Classify the preparation.
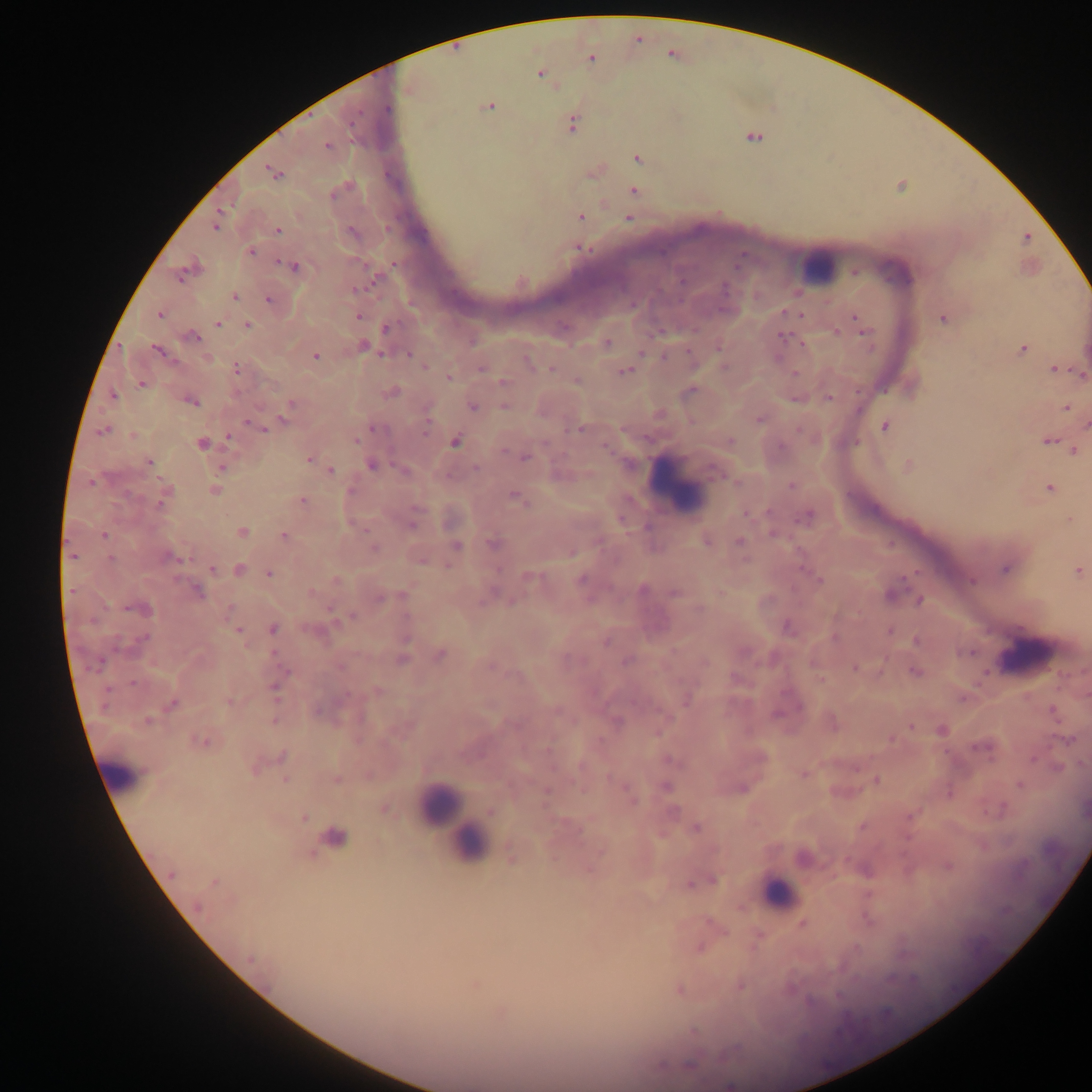

Thick blood film.

Approximate centers as x y in pixels. Leukocyte locations: 819 266; 679 483; 1025 656; 124 774; 439 805; 460 827; 469 844; 778 891. Malaria parasite locations: 591 59; 540 75; 487 107; 389 109; 350 124; 572 125; 754 137; 327 146; 638 159; 273 173; 634 192; 581 217; 628 219; 215 226; 278 230; 1027 238; 580 248; 251 252; 293 266; 855 271; 182 276; 374 280; 682 280; 725 289; 357 290; 234 297; 269 300; 786 313; 160 314; 799 314; 358 316; 857 318; 943 319; 218 324; 861 324; 248 326; 386 328; 837 331; 865 332; 192 336; 783 337; 607 343; 363 346; 718 348; 1023 350; 158 351; 641 353; 382 354; 408 354; 315 356; 664 357; 207 359; 528 363; 425 367; 237 368; 482 368; 552 368; 1054 368; 625 371; 794 374; 1081 374; 449 377; 504 381; 577 381; 141 383; 391 392; 113 396; 828 398; 192 402; 289 405; 504 405; 473 407; 1066 408; 285 419; 760 419; 253 425; 885 426; 427 427; 261 428; 373 429; 103 430; 579 430; 799 430; 134 436; 229 437; 356 440; 731 441; 1048 441; 455 442; 201 444; 1074 450; 309 458; 525 458; 149 462; 371 465; 908 467; 222 468; 476 468; 331 470; 404 471; 715 472; 91 482; 736 482; 792 485; 1050 487; 214 491; 517 498; 302 500; 161 503; 748 513; 808 515; 1070 519; 413 525; 243 532; 774 533; 104 535; 283 536; 706 542; 740 542; 494 544; 456 546; 374 548; 571 552; 73 556; 168 557; 111 558; 422 561; 448 566; 1005 568; 212 569; 239 569; 1078 571; 269 574; 529 577; 820 579; 580 580; 971 581; 643 590; 72 591; 196 592; 312 593; 673 593; 402 594; 891 594; 379 598; 920 600; 699 608; 143 609; 231 609; 352 616; 787 627; 273 629; 237 630; 890 632; 835 637; 142 639; 916 641; 605 642; 967 653; 440 656; 401 658; 626 661; 705 662; 97 665; 341 667; 854 668; 915 672; 133 683; 275 690; 376 691; 687 699; 229 702; 171 704; 1053 710; 316 711; 778 714; 618 721; 148 722; 912 727; 942 730; 891 739; 1068 739; 202 741; 981 748; 282 756; 1033 759; 671 761; 1057 768; 803 773; 337 779; 876 779; 285 780; 1019 785; 665 787; 742 788; 547 792; 630 795; 385 810; 490 812; 303 818; 862 826; 696 828; 334 837; 601 852; 512 858; 948 866; 171 874; 214 881; 714 881; 690 884; 198 907; 803 923; 701 948; 251 959; 474 984; 679 990; 694 1032; 690 1064; 661 1065. Image is 1092×1092 pixels. Single field of view. Photographed through a microscope with a mobile-phone camera. Sample from Ghana.